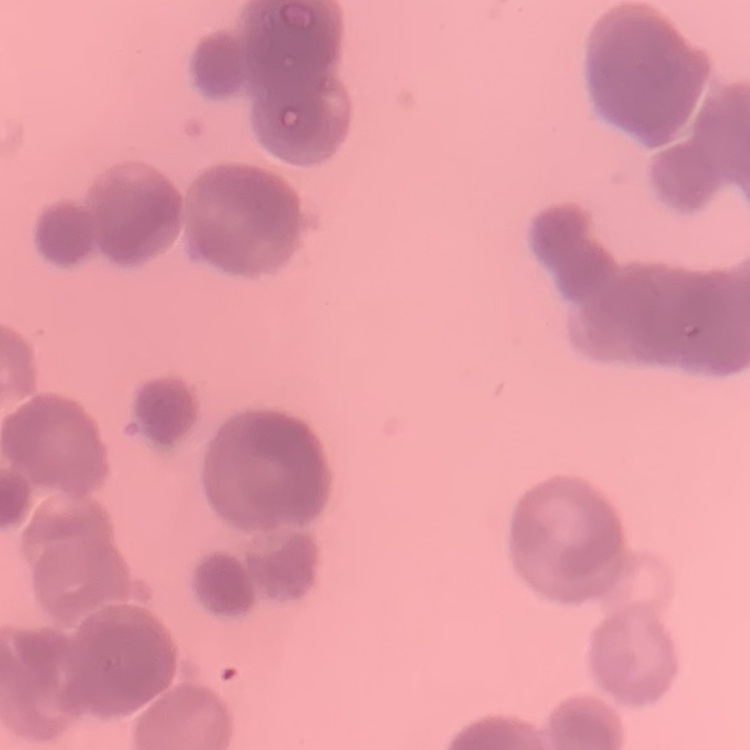

erythrocyte_morphology: rouleaux formation
preparation: thin peripheral smear
stain: Field's or Giemsa
image_type: square crop of a larger photomicrograph